State the blood parasite species.
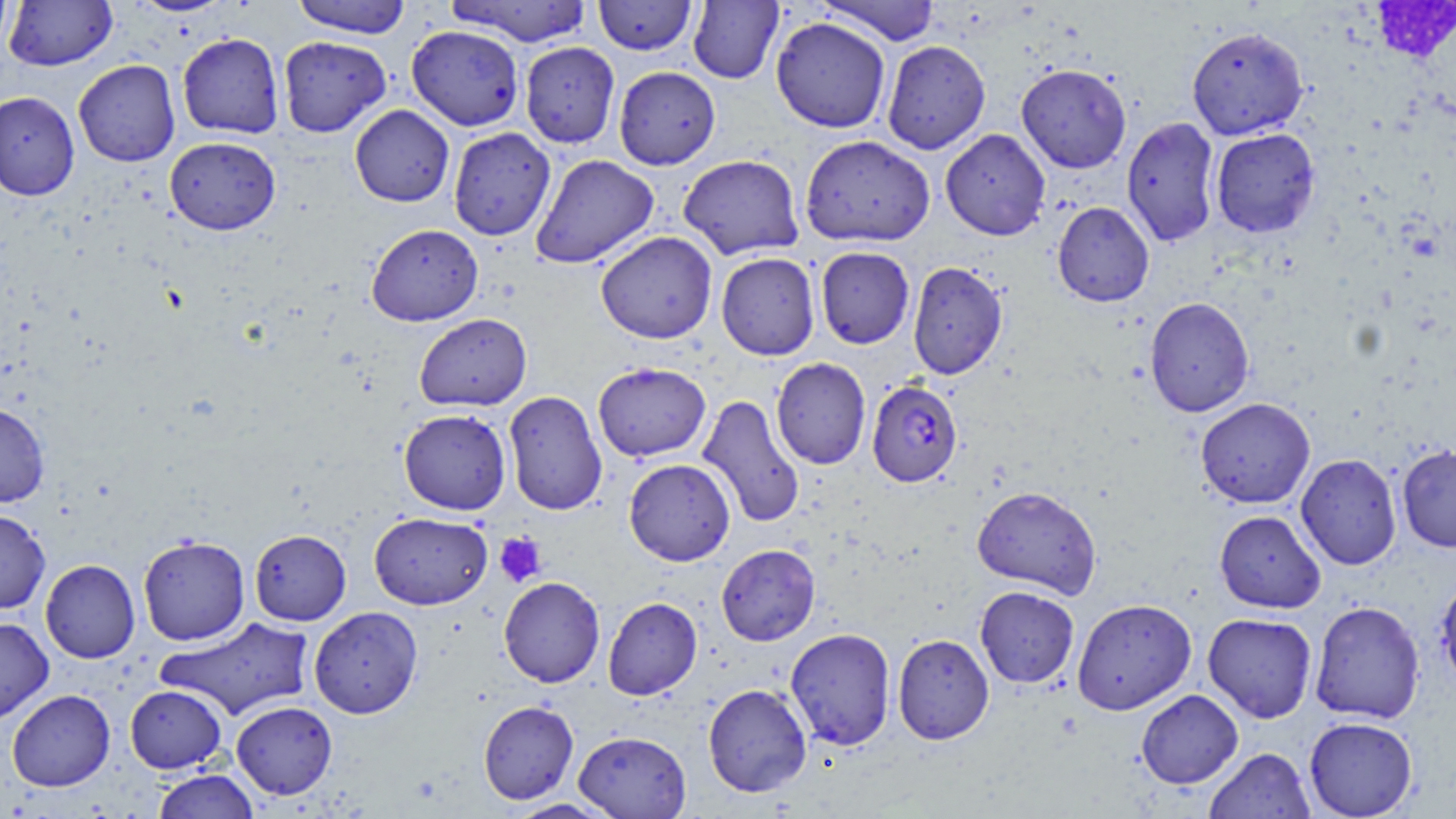
Plasmodium falciparum.

Approximate bounding boxes as (x1, y1, x2, y2) in pixels. Platelet locations: (494, 533, 547, 587). Uninfected red blood cell locations: (0, 0, 13, 55), (129, 0, 233, 17), (289, 0, 413, 38), (445, 0, 594, 46), (594, 0, 698, 56), (815, 0, 943, 45), (4, 1, 117, 71), (688, 1, 784, 84), (771, 17, 891, 133), (407, 25, 524, 131), (1187, 25, 1308, 140), (177, 32, 285, 139), (278, 36, 391, 137), (881, 40, 991, 154), (520, 41, 621, 148), (73, 60, 180, 167), (1016, 64, 1132, 173), (613, 65, 721, 170), (0, 91, 80, 200), (350, 104, 454, 207), (1121, 116, 1221, 247), (448, 127, 556, 241), (1210, 128, 1320, 237), (940, 129, 1050, 240), (800, 135, 935, 247), (164, 136, 281, 235), (530, 154, 659, 269), (678, 154, 804, 259), (1052, 201, 1154, 307), (366, 223, 483, 326), (595, 231, 718, 344), (815, 246, 914, 348), (716, 252, 820, 360), (907, 261, 1008, 379), (1144, 296, 1254, 417), (414, 313, 532, 411), (771, 357, 871, 470), (593, 361, 711, 462), (504, 390, 608, 516), (697, 394, 806, 529), (1195, 398, 1315, 508), (0, 402, 50, 507), (399, 408, 511, 515), (1397, 445, 1456, 552), (1296, 453, 1402, 570), (624, 458, 735, 566), (972, 485, 1102, 598), (0, 508, 50, 614), (1214, 510, 1326, 614), (369, 511, 492, 609), (249, 529, 351, 625), (138, 535, 250, 645), (716, 544, 820, 646), (40, 559, 140, 663), (1435, 572, 1456, 694), (498, 577, 605, 687), (975, 586, 1079, 688), (603, 597, 702, 700), (1072, 599, 1197, 714), (1309, 601, 1426, 724), (309, 606, 423, 718), (1203, 613, 1317, 723), (0, 616, 54, 724), (156, 616, 315, 721), (785, 627, 896, 750), (892, 633, 994, 744), (703, 684, 812, 797), (125, 685, 227, 773), (7, 689, 115, 791), (1136, 689, 1243, 788), (478, 700, 579, 804), (231, 701, 337, 799), (1304, 716, 1418, 818), (573, 730, 691, 818), (1204, 747, 1315, 819), (150, 769, 261, 819), (505, 799, 619, 818). Plasmodium falciparum-infected red blood cell locations: (867, 380, 963, 487). May-Grünwald-Giemsa stain. Light microscopy. 1000x magnification. Image is 1456×819 pixels. Thin blood film. One field of a larger specimen.